Comment on the morphology of the red blood cells.
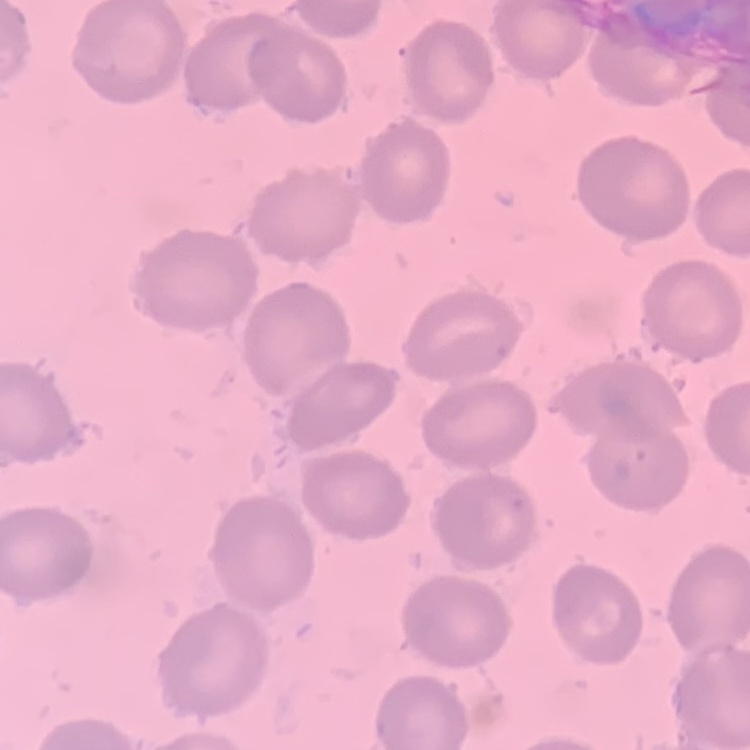

They show no rouleaux formation.

image type = square crop of a larger photomicrograph
stain = Field's or Giemsa
preparation = thin blood film